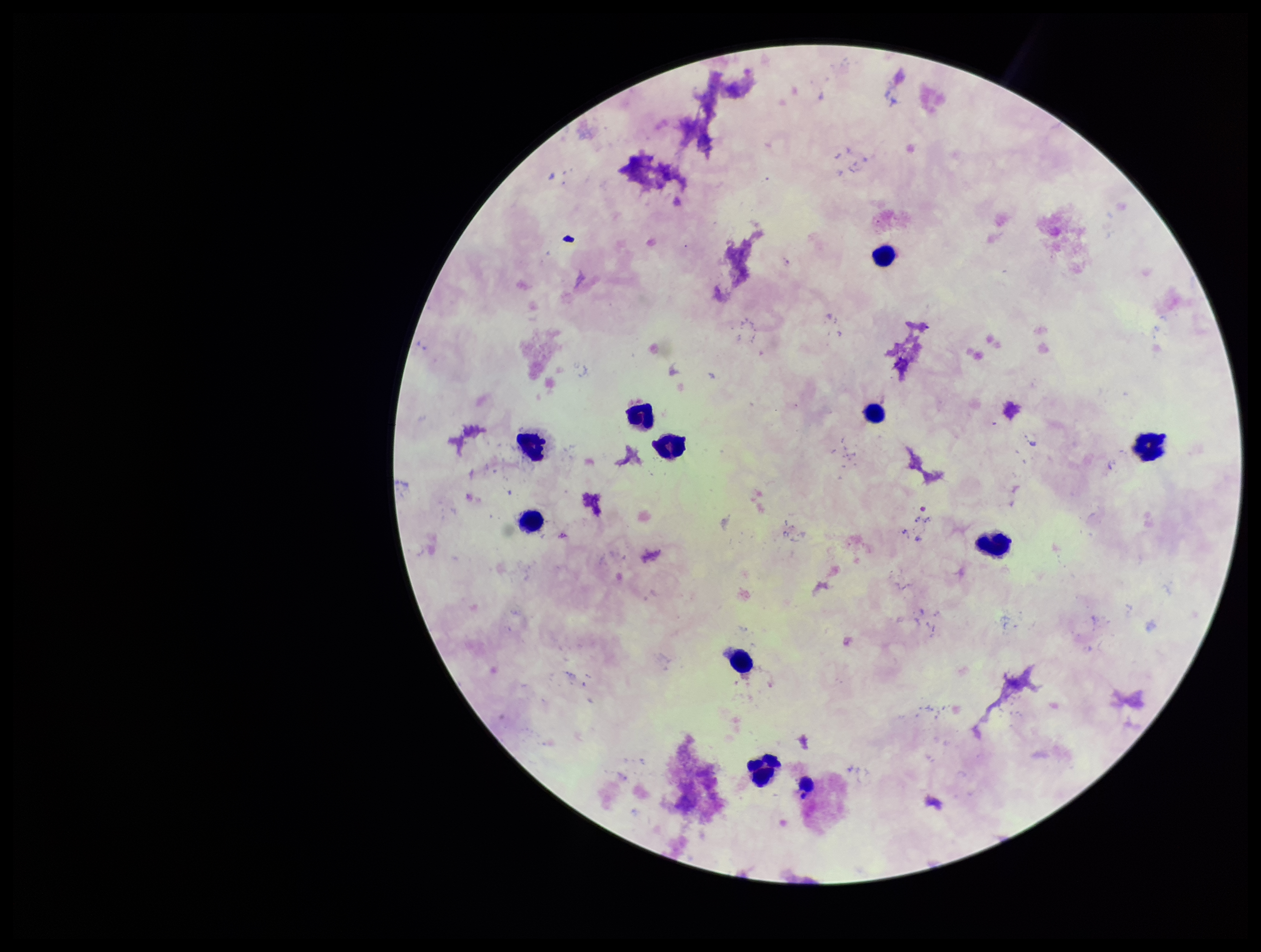 Single field of view. Parasite count: 0. Smartphone photograph taken through the eyepiece of a microscope. Plasmodium parasites: none identified. Image is 1261×952 pixels. Stained with Giemsa. Leukocyte count: 10. Preparation: thick. Patient malaria status: negative.